Assess this cell for malaria.
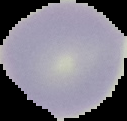
It is uninfected.

Image is 127×121 pixels. Cell region segmented out of the field of view; the surrounding area is masked to black. From a thin blood film.